Name the cell type shown.
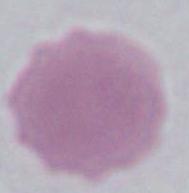

This is an erythrocyte.

modality: micrograph
magnification: 1000x